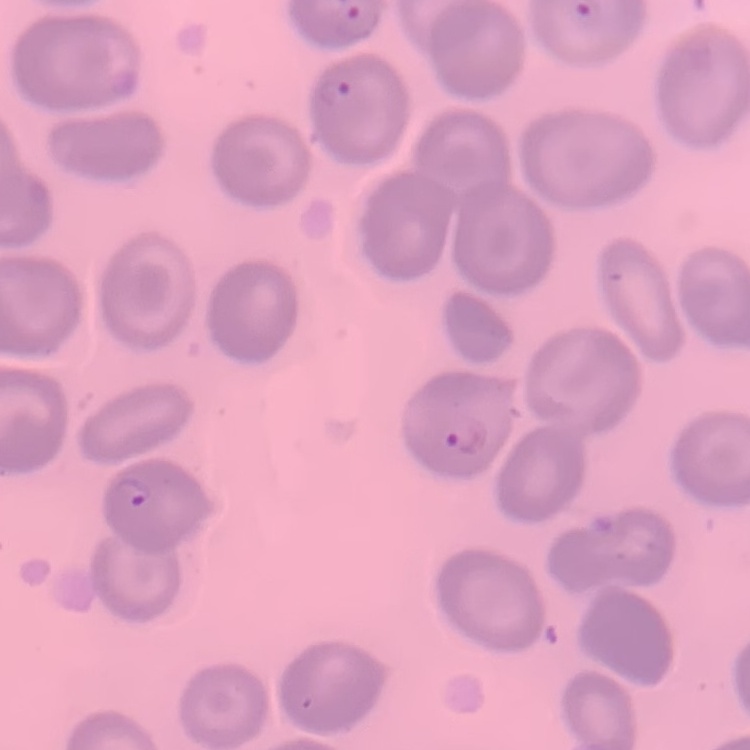 The red blood cells exhibit no rouleaux formation. Square crop of a larger photomicrograph. Thin peripheral smear. Field's or Giemsa stain.